Locate and identify every blood parasite.
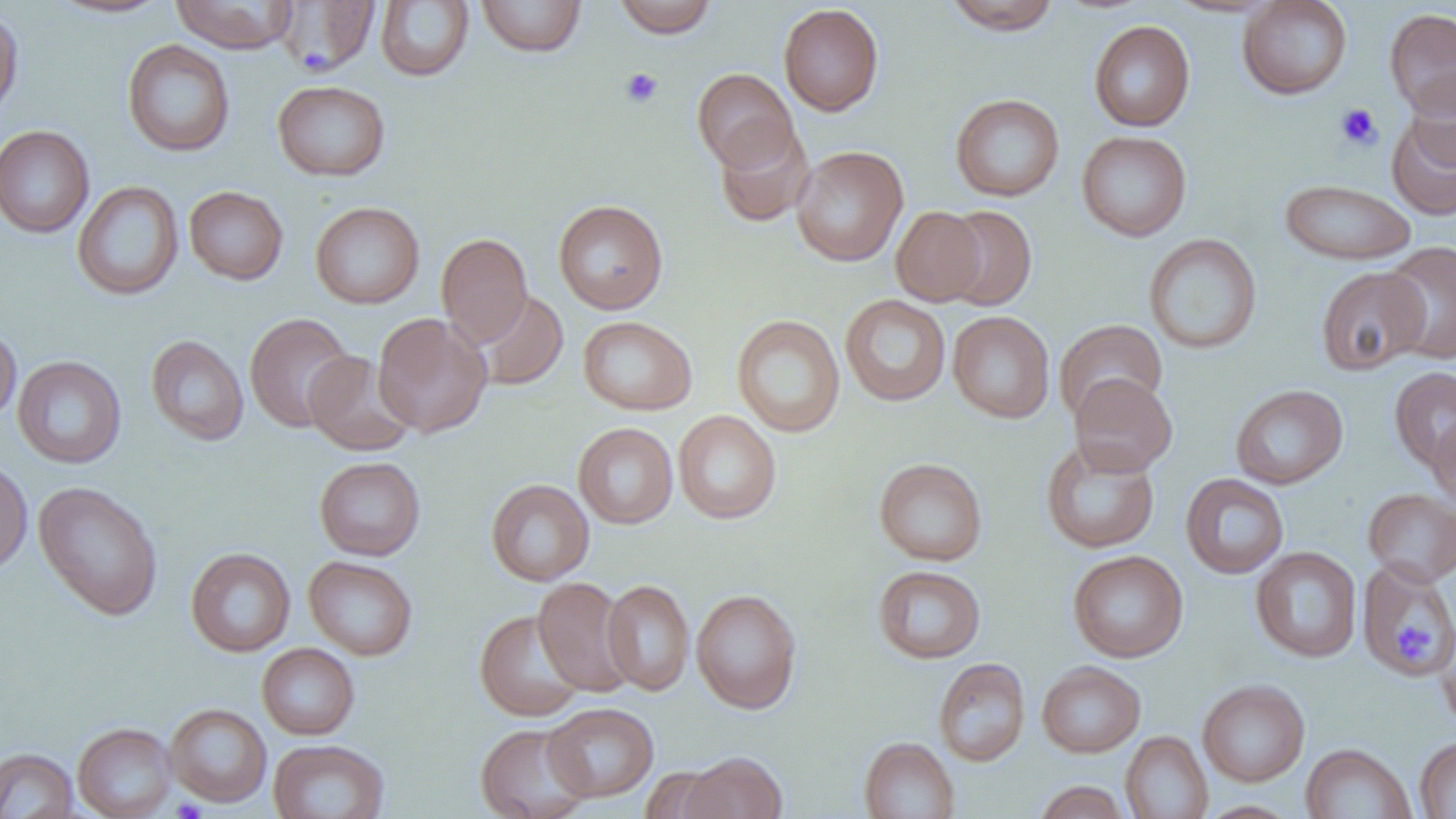
No blood parasites seen.

Approximate bounding boxes as (x1,y1)-(x2,y2) corner pairs in pixels. Uninfected red blood cell locations: (47,0)-(175,18), (169,0)-(299,53), (273,0)-(381,76), (476,0)-(587,57), (613,0)-(719,38), (1237,0)-(1353,100), (375,1)-(474,82), (943,1)-(1061,35), (778,3)-(884,116), (0,8)-(24,124), (1384,8)-(1456,118), (1089,20)-(1195,132), (122,40)-(236,157), (692,68)-(798,172), (1404,68)-(1456,173), (272,80)-(391,181), (950,94)-(1065,201), (1386,111)-(1456,221), (713,120)-(814,228), (0,125)-(95,238), (1076,130)-(1192,242), (791,145)-(908,267), (1278,178)-(1418,266), (72,181)-(184,300), (184,185)-(288,285), (553,199)-(668,315), (310,201)-(425,308), (940,205)-(1037,311), (891,206)-(987,306), (436,233)-(533,347), (1143,233)-(1262,354), (1380,241)-(1456,365), (1315,265)-(1429,376), (472,290)-(569,390), (840,294)-(951,407), (947,311)-(1055,423), (373,312)-(492,438), (244,313)-(357,432), (731,314)-(845,438), (578,316)-(697,415), (1053,319)-(1168,423), (0,326)-(21,426), (146,334)-(249,446), (304,351)-(416,456), (13,355)-(126,469), (1389,365)-(1456,471), (1070,374)-(1177,477), (1230,384)-(1348,490), (672,410)-(782,524), (1427,412)-(1456,511), (573,422)-(678,529), (1040,440)-(1160,554), (314,456)-(426,561), (0,457)-(33,577), (874,457)-(988,566), (1180,473)-(1289,579), (486,478)-(595,586), (32,481)-(164,621), (1363,488)-(1456,586), (1250,546)-(1362,663), (185,547)-(296,657), (1067,550)-(1188,663), (303,556)-(417,661), (1356,560)-(1456,679), (872,564)-(986,664), (533,577)-(636,696), (602,579)-(694,695), (690,588)-(802,714), (474,610)-(588,722), (1433,617)-(1456,734), (257,643)-(360,740), (933,657)-(1030,767), (1036,661)-(1146,758), (1197,679)-(1310,786), (543,702)-(658,802), (165,703)-(272,807), (73,722)-(177,819), (476,723)-(593,819), (1120,731)-(1213,818), (859,736)-(960,818), (1415,736)-(1456,818), (268,738)-(390,819), (1300,743)-(1417,819), (0,747)-(79,818), (680,751)-(787,818), (639,766)-(730,819), (1033,780)-(1131,819), (1197,801)-(1300,819). Platelet locations: (619,67)-(663,108), (1335,103)-(1383,151), (1399,624)-(1431,661), (172,798)-(206,819). Slide-level diagnosis: negative for blood parasites. 1000x magnification. Thin blood film. Single field of view. Image is 1456×819 pixels. Light microscopy.